Classify this cell by malaria status.
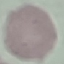
It is uninfected.

stain: Giemsa
preparation: thin smear
capture: smartphone through the microscope eyepiece
image_type: cell patch, automatically extracted from a larger field of view and resized to 64 × 64 pixels